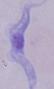
Summary:
  - Magnification: 1000x
  - Identification: trypanosome
  - Modality: photomicrograph